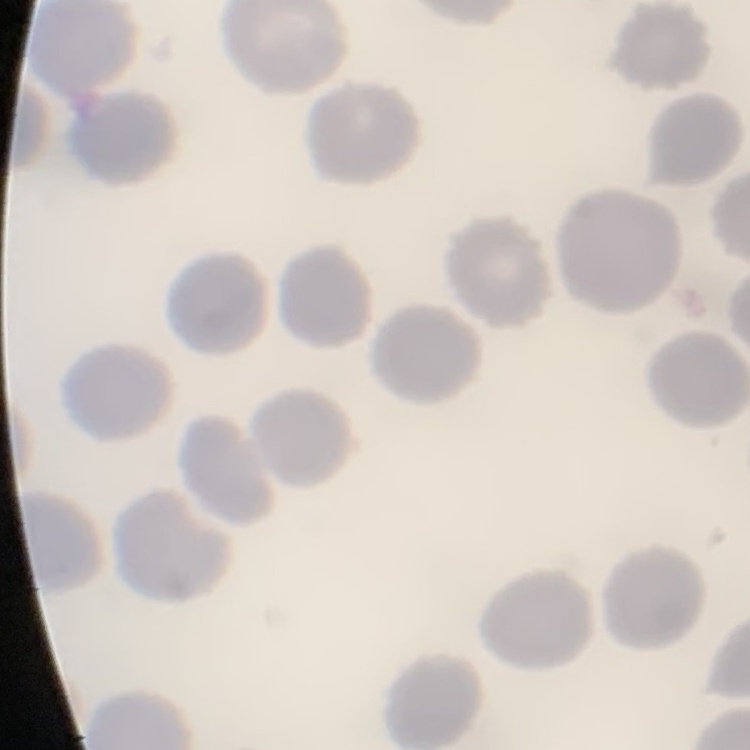 The erythrocytes show no rouleaux formation. Square crop of a larger photomicrograph. Thin peripheral smear. Stained with either Field's or Giemsa.